Report the malaria status of this cell.
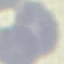

Uninfected.

Summary:
  - Preparation: thin blood smear
  - Capture: smartphone through the microscope eyepiece
  - Image type: automatically extracted cell patch, resized to 64 × 64 pixels
  - Stain: Giemsa